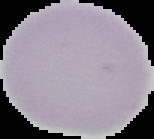 Image is 154×139 pixels. From a thin blood film. Result: no Plasmodium parasites detected. Segmented cell region on a black background.